State which parasite is depicted.
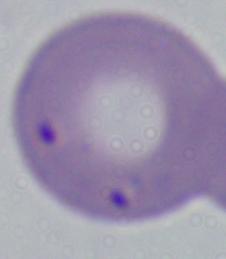

Babesia.

Summary:
  - Magnification: 1000x
  - Modality: photomicrograph